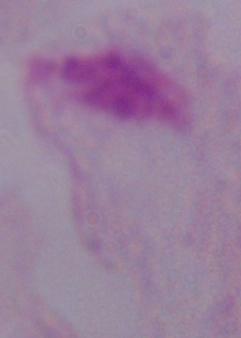 Micrograph. A trichomonad is seen. Captured at 1000x magnification.